Assess for malaria.
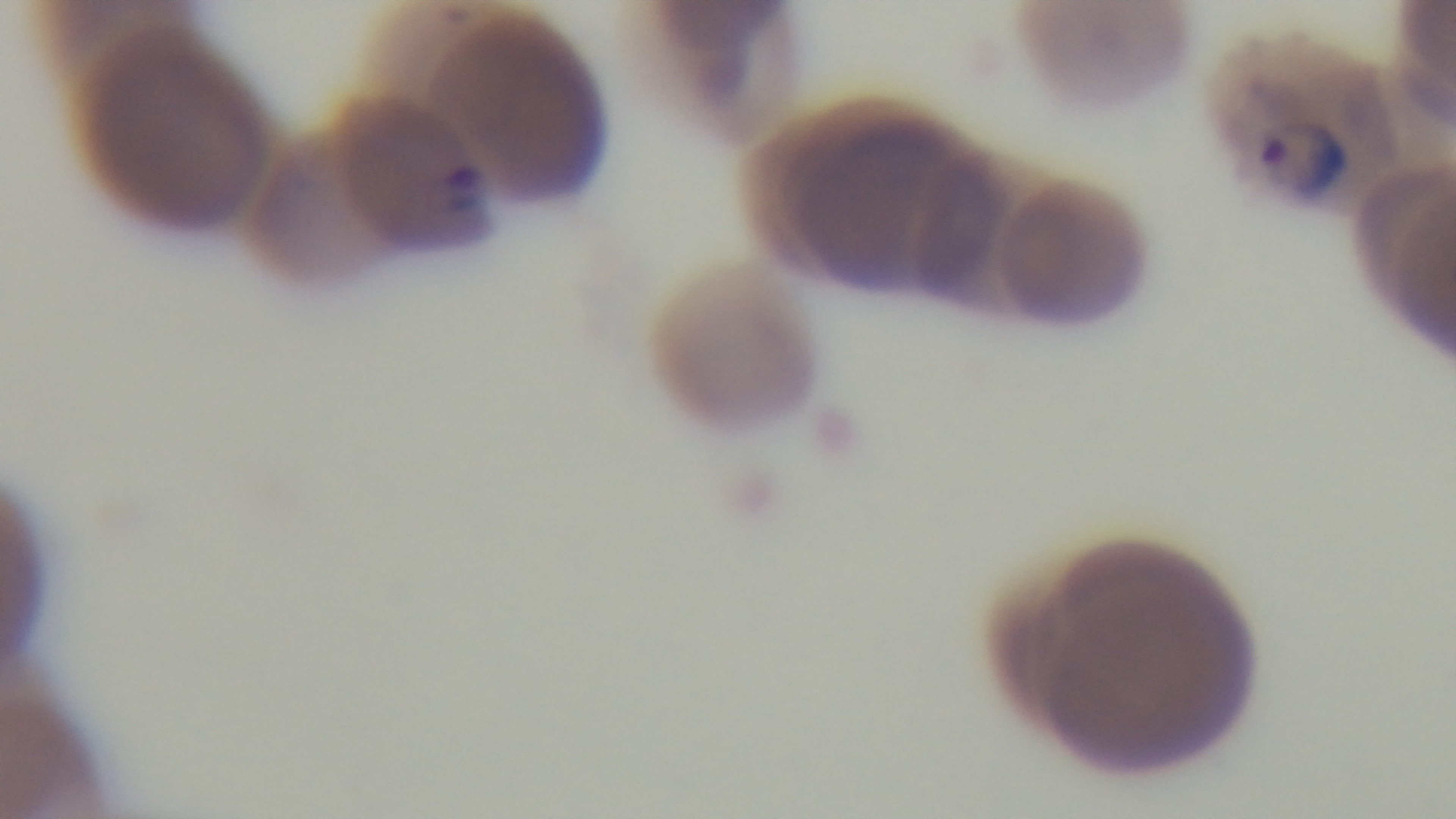
Positive.

modality = light microscopy
field of view = one from the slide
capture = mounted 4K digital camera
objective = 100x oil immersion
preparation = thin
stain = Giemsa